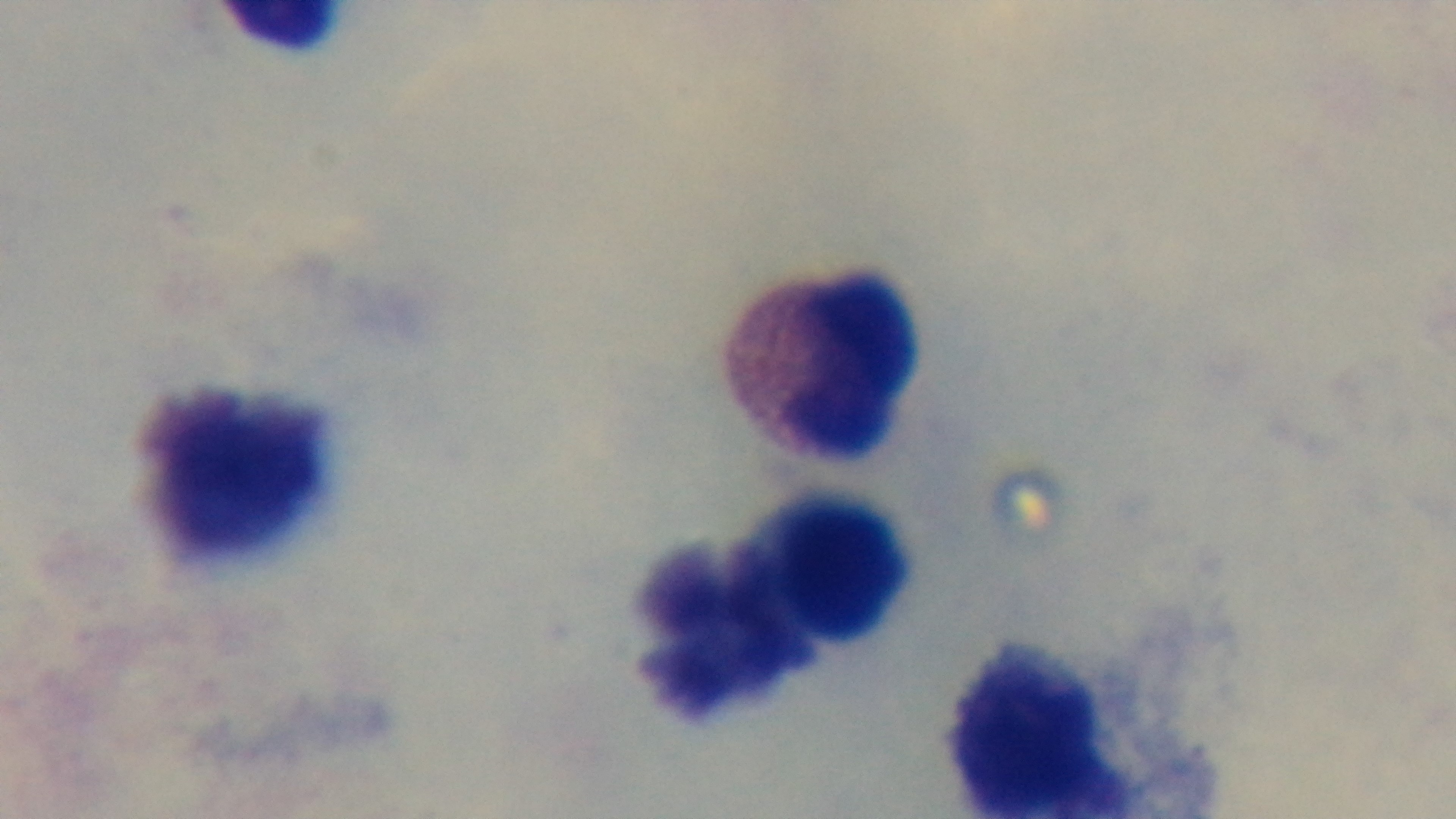
Summary:
  - Malaria status: uninfected
  - Preparation: thick
  - Stain: Giemsa
  - Field of view: one from the slide
  - Objective: 100x oil immersion
  - Capture: mounted 4K digital camera
  - Modality: light microscopy